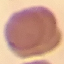
Summary:
  - Result: no malaria parasites seen
  - Preparation: thin blood film
  - Image type: automatically extracted cell patch, resized to 64 × 64 pixels
  - Stain: Giemsa
  - Capture: smartphone through the microscope eyepiece